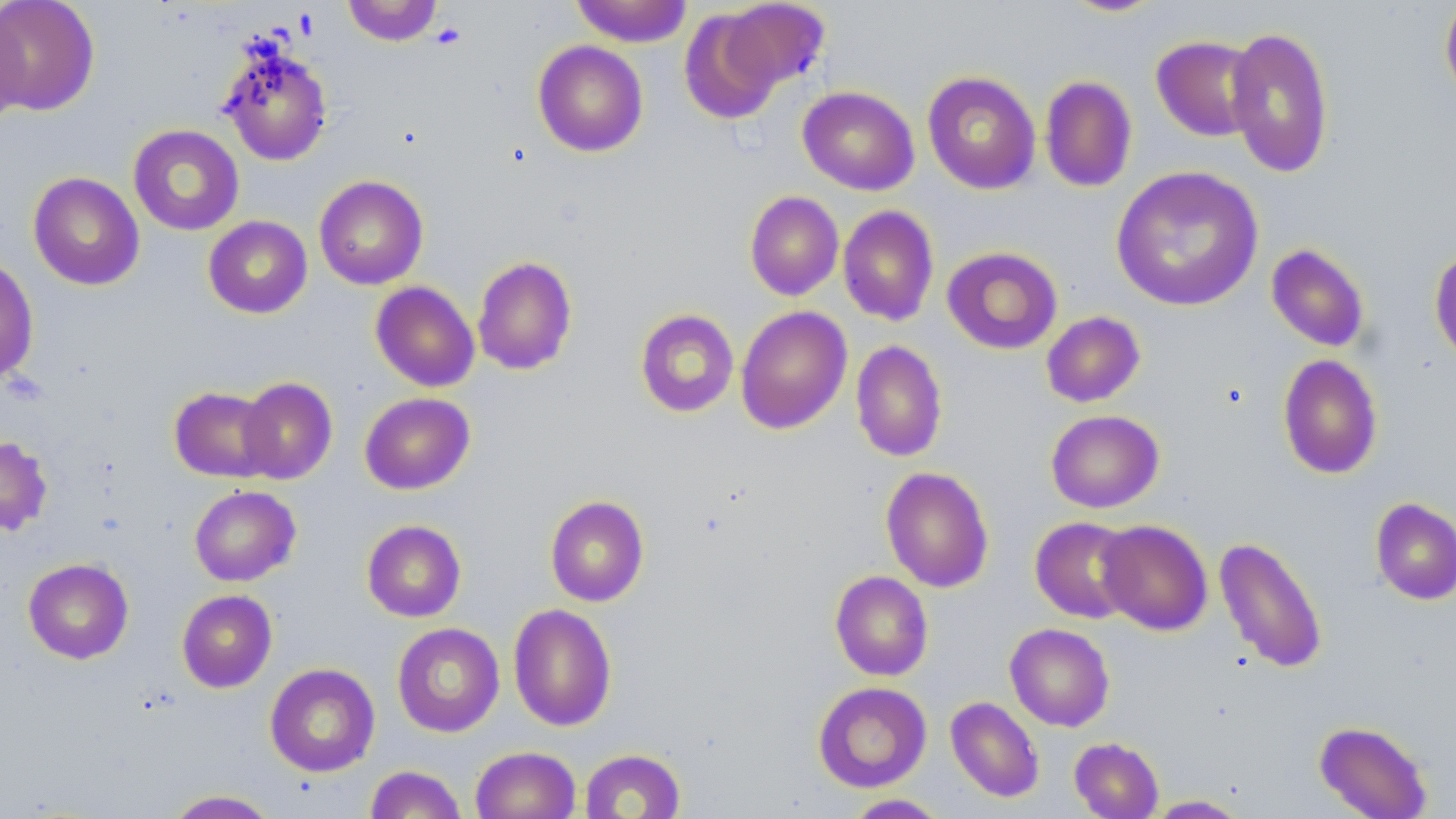

slide-level diagnosis = negative for blood parasites
field of view = one of a larger specimen
modality = optical microscopy
magnification = 1000x
preparation = thin blood film
uninfected red blood cell locations = approximate bounding boxes as (x1,y1)-(x2,y2) corner pairs in pixels: (0,0)-(101,116), (342,0)-(442,46), (571,0)-(693,47), (1059,0)-(1168,17), (718,1)-(830,92), (1439,1)-(1456,107), (0,6)-(28,128), (679,8)-(786,125), (1225,25)-(1335,179), (1151,35)-(1262,142), (217,38)-(333,167), (532,40)-(648,157), (922,71)-(1041,195), (1039,75)-(1138,192), (797,86)-(919,195), (128,124)-(244,235), (1111,165)-(1263,312), (28,172)-(144,290), (314,175)-(428,290), (744,191)-(844,301), (838,205)-(939,326), (203,216)-(312,318), (1265,243)-(1370,352), (1429,245)-(1456,367), (942,246)-(1063,354), (472,255)-(578,375), (0,257)-(39,384), (370,281)-(480,392), (735,305)-(852,435), (635,309)-(739,417), (1041,311)-(1145,408), (851,340)-(947,462), (1277,354)-(1384,479), (236,377)-(338,484), (169,386)-(278,482), (359,393)-(475,494), (1046,410)-(1164,513), (0,436)-(53,536), (880,466)-(994,593), (189,485)-(301,586), (545,495)-(649,607), (1370,497)-(1456,605), (1030,516)-(1139,623), (361,519)-(466,622), (1097,520)-(1213,635), (1213,536)-(1329,674), (23,557)-(134,664), (830,570)-(933,681), (176,589)-(277,692), (508,603)-(617,732), (392,623)-(504,737), (1005,623)-(1115,731), (265,663)-(380,777), (813,681)-(932,792), (945,696)-(1045,803), (1313,720)-(1433,818), (1069,737)-(1163,818), (470,746)-(581,819), (580,748)-(686,819), (364,760)-(580,818), (364,765)-(467,819), (163,789)-(279,818), (843,794)-(950,818), (1144,795)-(1250,818)
stain = May-Grünwald-Giemsa
platelet locations = approximate bounding boxes as (x1,y1)-(x2,y2) corner pairs in pixels: (431,23)-(466,49)
image size = 1456×819 pixels